Report the malaria status of this cell.
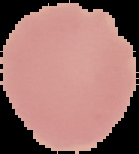
It is uninfected.

From a thin blood film. Image is 139×154 pixels. The area outside the segmented cell region is set to black.